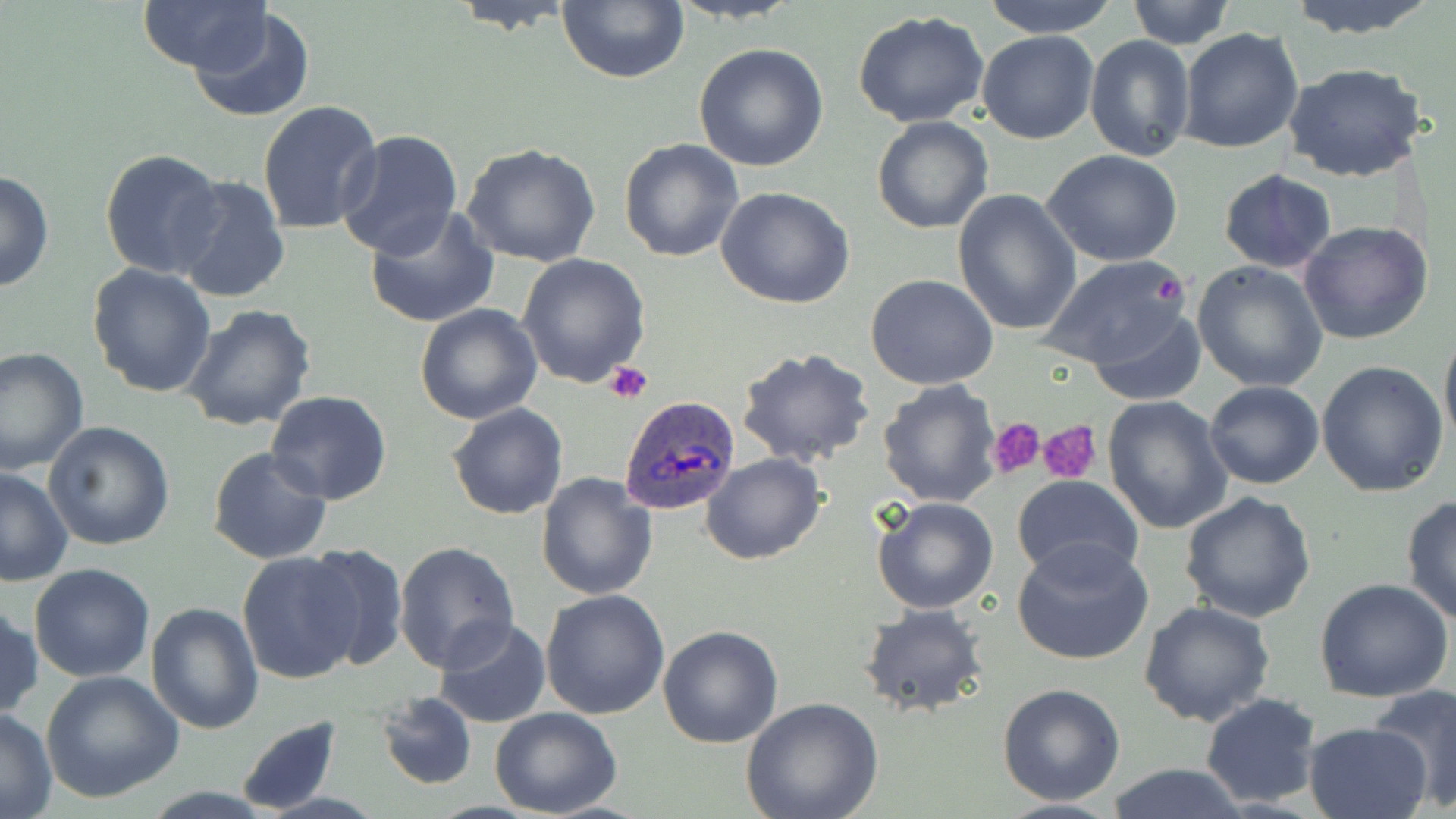

Summary:
  - Coordinate format: approximate bounding boxes as (x1,y1)-(x2,y2) corner pairs in pixels
  - Uninfected red blood cell locations: (138,0)-(268,76), (979,0)-(1120,36), (1124,0)-(1238,49), (1282,0)-(1443,40), (445,1)-(577,33), (556,1)-(690,84), (187,7)-(315,123), (852,11)-(992,129), (1178,27)-(1304,154), (977,31)-(1101,144), (1085,35)-(1194,160), (694,44)-(829,172), (1282,62)-(1430,184), (257,101)-(383,235), (871,116)-(994,235), (334,128)-(465,261), (618,139)-(743,262), (459,141)-(602,267), (99,148)-(227,281), (1041,148)-(1184,268), (1220,169)-(1337,272), (0,170)-(54,293), (169,174)-(291,304), (715,186)-(856,309), (951,187)-(1083,336), (364,205)-(499,330), (1298,219)-(1435,345), (516,253)-(651,387), (1038,254)-(1193,371), (1191,260)-(1330,392), (87,263)-(218,398), (866,274)-(998,390), (415,303)-(542,424), (178,304)-(316,431), (1087,307)-(1204,402), (1439,329)-(1456,450), (0,346)-(89,475), (735,347)-(875,469), (1316,361)-(1449,497), (876,379)-(1003,507), (1205,380)-(1324,489), (265,390)-(393,505), (1102,395)-(1234,534), (446,403)-(567,520), (43,421)-(176,551), (207,446)-(333,565), (700,454)-(823,566), (1,468)-(75,587), (536,473)-(658,600), (1012,475)-(1143,583), (1178,492)-(1318,624), (1400,493)-(1456,626), (871,496)-(999,615), (1012,538)-(1154,667), (394,542)-(520,671), (301,543)-(408,671), (237,551)-(367,685), (29,563)-(158,682), (1314,578)-(1456,703), (541,588)-(672,720), (1137,599)-(1277,727), (0,600)-(41,721), (147,602)-(264,735), (858,603)-(989,717), (433,617)-(553,730), (658,626)-(784,748), (40,670)-(184,803), (997,683)-(1128,806), (1368,684)-(1456,809), (376,692)-(477,790), (1200,692)-(1324,809), (741,698)-(885,819), (0,706)-(58,818), (490,706)-(624,818), (234,717)-(341,817), (1301,721)-(1432,819), (1106,763)-(1248,819), (988,799)-(1130,818)
  - Plasmodium ovale-infected red blood cell locations: (619,396)-(740,516)
  - Platelet locations: (1154,275)-(1183,304), (604,362)-(653,404), (988,420)-(1046,481), (1036,420)-(1101,484)
  - Slide-level diagnosis: Plasmodium ovale
  - Image size: 1456×819 pixels
  - Field of view: one of a larger specimen
  - Magnification: 1000x
  - Preparation: thin blood smear
  - Stain: May-Grünwald-Giemsa
  - Modality: light microscopy